State which parasite is depicted.
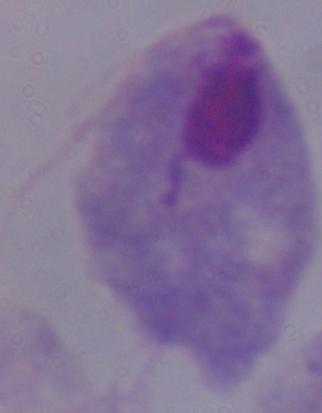

This is a trichomonad.

Photomicrograph. Captured at 1000x magnification.